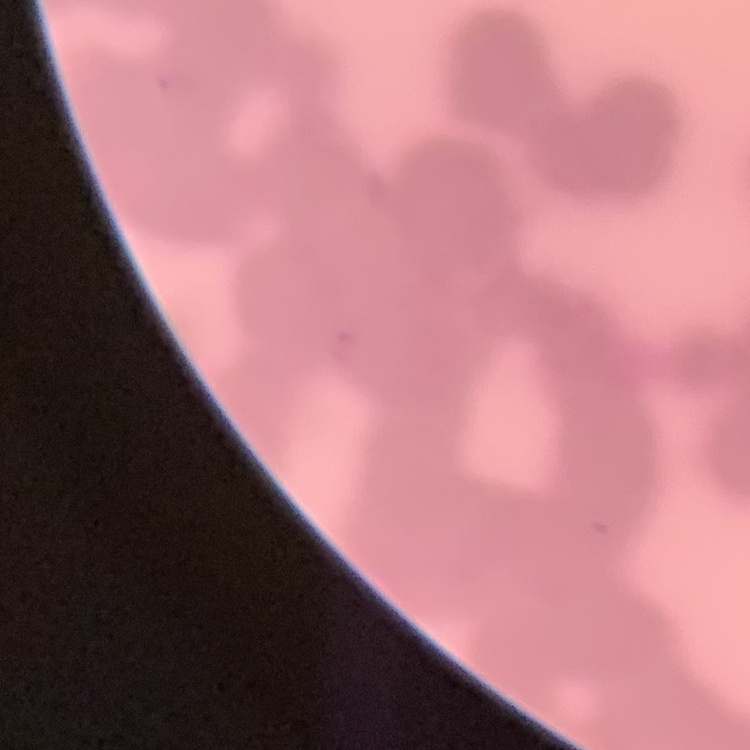
The erythrocytes show rouleaux formation. One tile cut from a larger photomicrograph. Thin blood smear. Field's or Giemsa stain.